Outline each Plasmodium ovale-infected red blood cell.
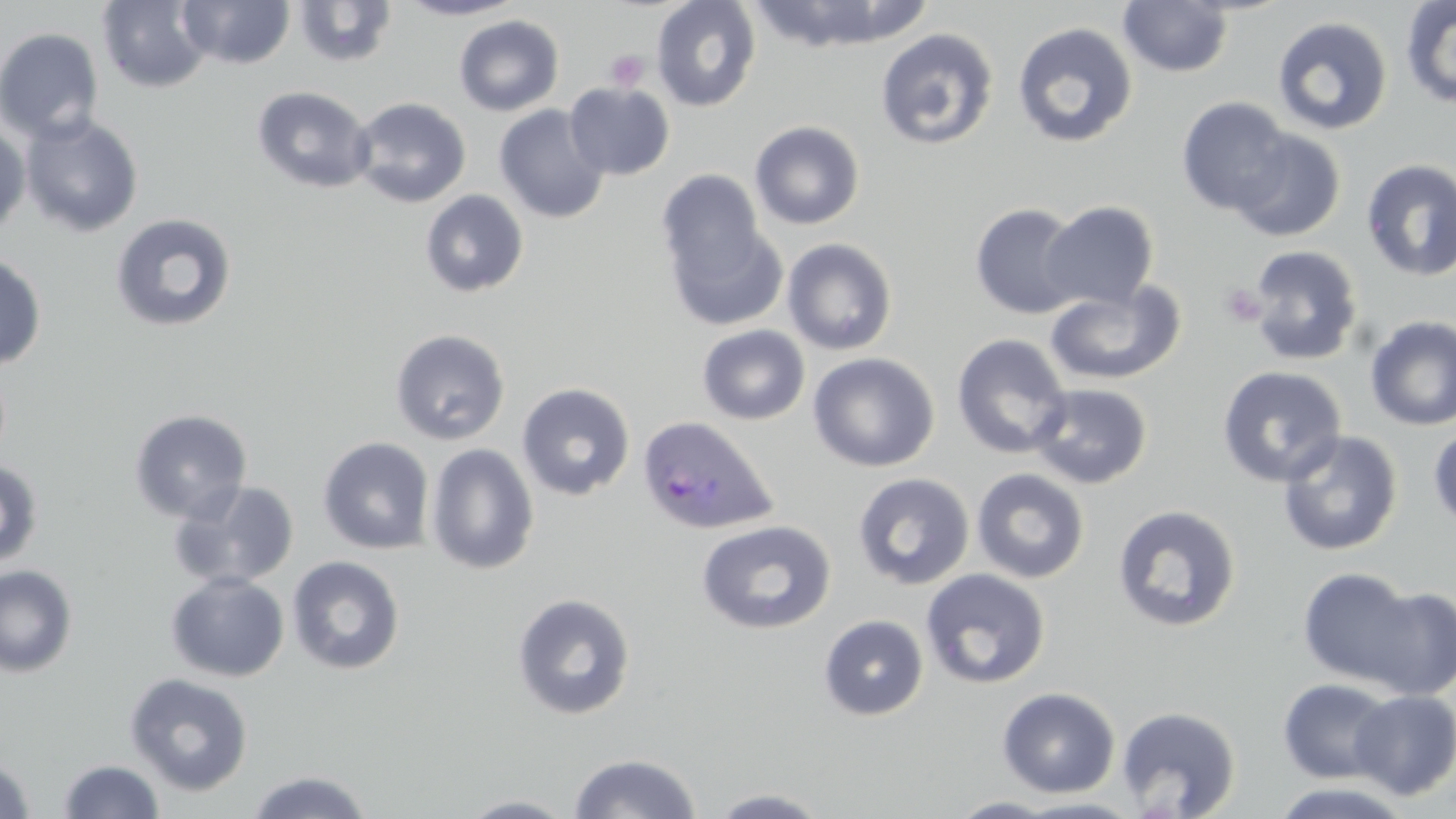

Approximate bounding boxes as [x1, y1, x2, y2] in pixels.
Plasmodium ovale-infected red blood cells: [637, 415, 779, 537].

slide_level_diagnosis: Plasmodium ovale
platelet_locations: 'approximate bounding boxes as [x1, y1, x2, y2] in pixels: [604, 50, 649, 91], [1219, 283, 1266, 326]'
image_size: 1456×819 pixels
uninfected_red_blood_cell_locations: 'approximate bounding boxes as [x1, y1, x2, y2] in pixels: [97, 0, 213, 93], [178, 0, 295, 69], [293, 0, 398, 69], [395, 0, 527, 21], [651, 0, 761, 112], [748, 0, 931, 52], [1117, 0, 1235, 77], [1400, 0, 1456, 109], [453, 14, 564, 116], [1272, 16, 1393, 135], [1012, 22, 1138, 148], [0, 26, 105, 143], [874, 27, 999, 151], [565, 81, 674, 180], [252, 86, 375, 195], [350, 97, 471, 208], [1176, 97, 1293, 216], [494, 104, 611, 224], [21, 112, 144, 238], [749, 120, 865, 230], [0, 122, 30, 239], [1228, 129, 1346, 242], [1360, 159, 1456, 281], [656, 170, 768, 288], [420, 189, 529, 298], [1040, 200, 1159, 310], [970, 202, 1085, 320], [110, 213, 237, 333], [661, 214, 788, 333], [781, 238, 898, 355], [1246, 244, 1363, 366], [0, 252, 47, 370], [1045, 281, 1187, 386], [1364, 315, 1456, 431], [697, 324, 810, 425], [389, 329, 510, 445], [951, 333, 1072, 459], [808, 352, 939, 472], [1216, 365, 1348, 488], [1028, 382, 1153, 490], [517, 383, 635, 500], [129, 408, 252, 523], [1428, 421, 1456, 534], [1276, 430, 1404, 557], [318, 437, 435, 555], [426, 443, 540, 575], [0, 459, 44, 571], [971, 468, 1090, 584], [852, 473, 975, 591], [168, 478, 300, 590], [1112, 504, 1242, 633], [696, 519, 837, 635], [287, 555, 405, 675], [0, 564, 78, 678], [1296, 567, 1426, 690], [920, 569, 1050, 689], [165, 572, 289, 682], [1357, 584, 1456, 700], [511, 592, 636, 720], [818, 615, 929, 720], [124, 672, 254, 797], [1277, 678, 1397, 783], [996, 687, 1121, 798], [1349, 690, 1456, 800], [1115, 705, 1241, 817], [567, 752, 703, 818], [0, 756, 37, 819], [56, 759, 165, 818], [244, 770, 375, 818], [1267, 781, 1419, 819], [707, 787, 834, 817], [454, 794, 581, 818], [949, 796, 1064, 818], [1013, 797, 1148, 817]'
modality: optical microscopy
preparation: thin blood film
magnification: 1000x
field_of_view: single
stain: May-Grünwald-Giemsa